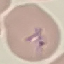

Summary:
  - Malaria status: parasitized
  - Preparation: thin blood film
  - Stain: Giemsa
  - Capture: smartphone camera at the microscope eyepiece
  - Image type: automatically extracted cell patch, resized to 64 × 64 pixels